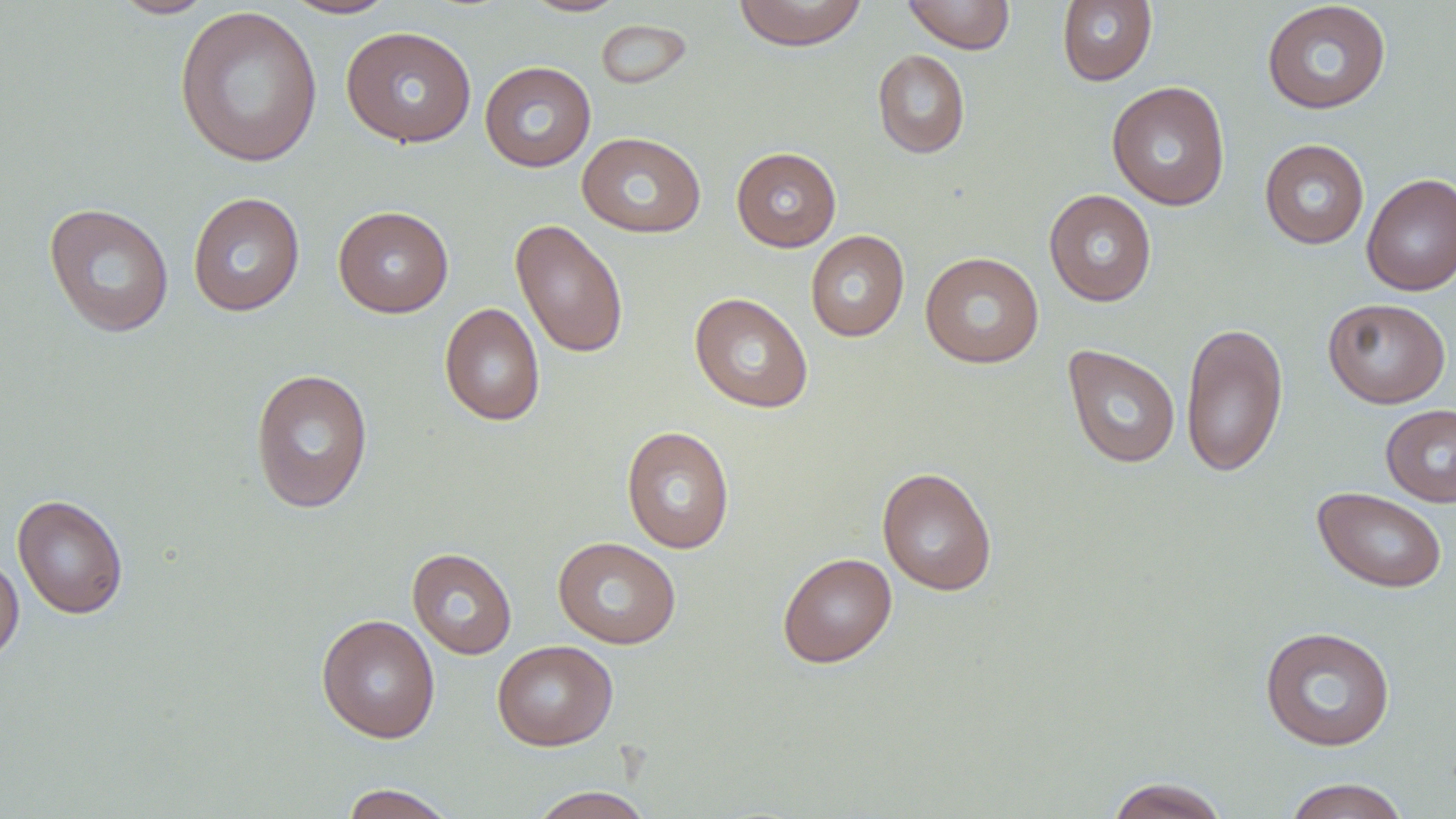

Approximate bounding boxes as [x1, y1, x2, y2] in pixels. Uninfected red blood cell locations: [109, 0, 218, 19], [280, 0, 399, 20], [519, 0, 630, 18], [732, 0, 869, 51], [903, 0, 1015, 54], [1056, 0, 1157, 86], [1261, 1, 1392, 114], [174, 6, 323, 167], [595, 18, 693, 91], [340, 25, 477, 148], [872, 49, 970, 159], [480, 61, 596, 172], [1107, 81, 1231, 211], [576, 132, 707, 238], [1259, 138, 1369, 249], [731, 147, 842, 252], [1362, 172, 1456, 296], [1044, 189, 1157, 306], [187, 191, 305, 316], [43, 202, 174, 337], [333, 205, 453, 317], [510, 219, 629, 358], [805, 230, 910, 342], [919, 252, 1045, 369], [689, 292, 814, 413], [1323, 298, 1451, 408], [439, 302, 545, 426], [1180, 321, 1288, 478], [1063, 345, 1180, 468], [249, 368, 375, 513], [1380, 404, 1456, 506], [621, 425, 735, 554], [877, 467, 997, 596], [1312, 487, 1448, 593], [12, 494, 128, 619], [553, 536, 682, 649], [406, 548, 517, 659], [0, 551, 24, 667], [777, 552, 897, 668], [316, 613, 440, 743], [1259, 625, 1396, 752], [492, 640, 618, 751], [1105, 776, 1231, 819], [1282, 777, 1411, 819], [340, 783, 459, 818], [526, 786, 656, 819]. Slide-level diagnosis: no evidence of blood parasites. Captured at 1000x magnification. Image is 1456×819 pixels. Thin blood film. May-Grünwald-Giemsa stain. One field of a larger specimen. Light microscopy.